Identify the parasite.
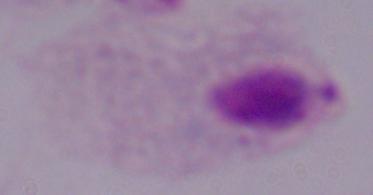

A trichomonad.

Photomicrograph. 1000x magnification.